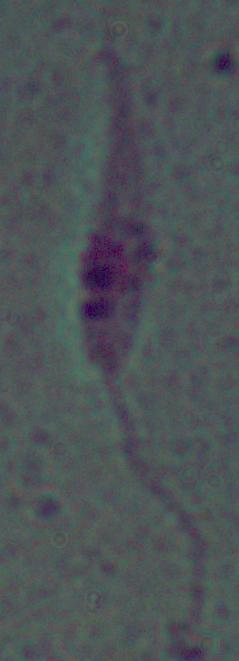

magnification = 1000x
identification = Leishmania
modality = micrograph